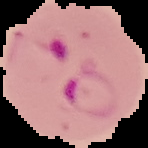

preparation: thin blood film
result: malaria parasites identified
image_size: 148×148 pixels
image_type: segmented cell region with the area outside set to black